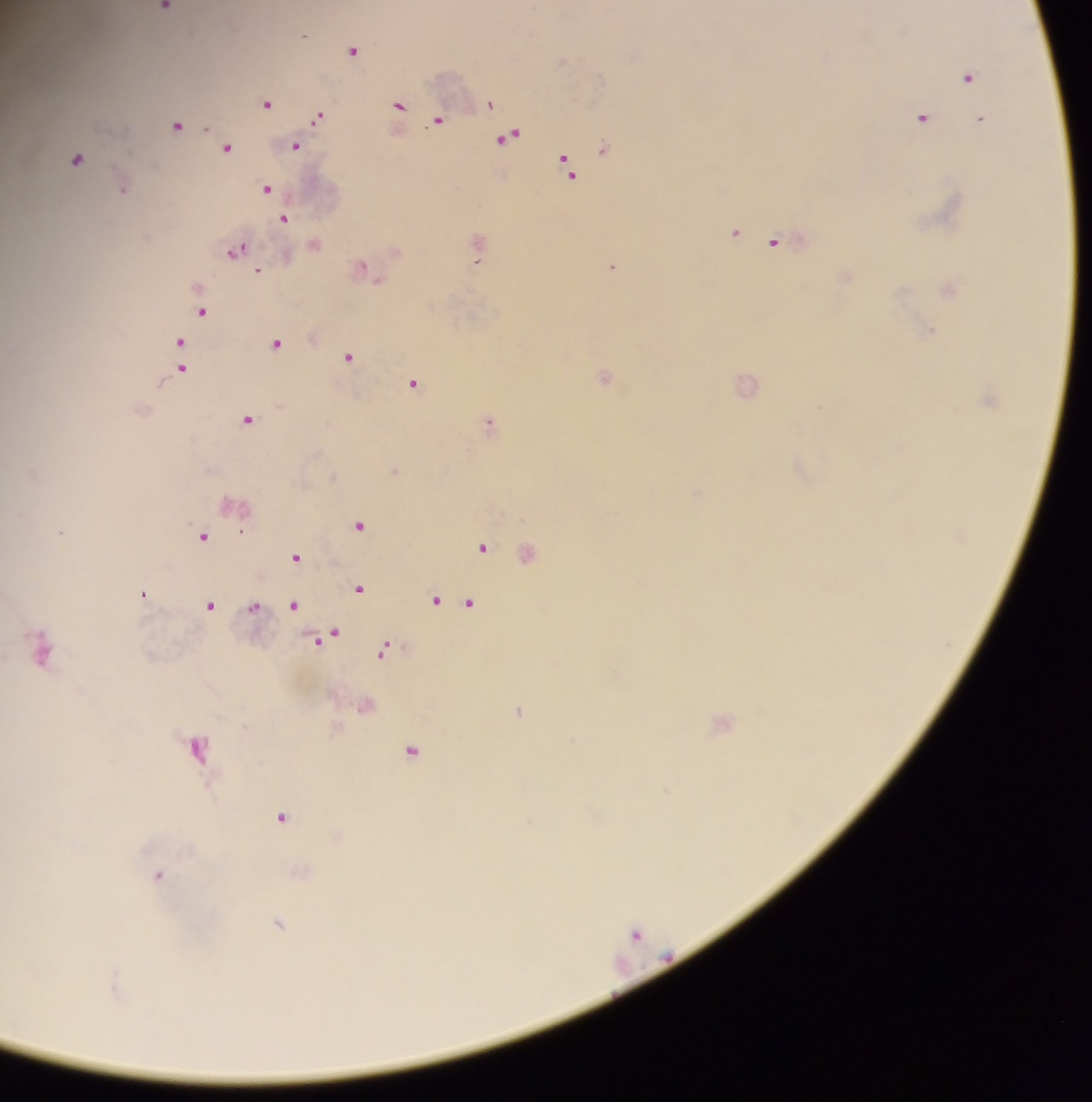
plasmodium_parasite_locations: 'approximate centers as [x, y] in pixels: [165, 8], [305, 36], [353, 51], [968, 77], [267, 104], [491, 104], [400, 105], [319, 116], [922, 118], [981, 119], [439, 120], [177, 125], [508, 137], [295, 147], [604, 147], [227, 148], [77, 160], [568, 165], [267, 189], [123, 190], [285, 219], [736, 232], [775, 242], [237, 250], [477, 263], [613, 266], [364, 268], [259, 272], [203, 312], [277, 343], [178, 344], [181, 357], [349, 357], [181, 369], [605, 377], [414, 383], [747, 384], [248, 419], [490, 423], [360, 526], [241, 531], [61, 532], [204, 536], [483, 548], [296, 557], [359, 589], [143, 594], [437, 600], [471, 602], [294, 605], [210, 606], [254, 607], [329, 637], [41, 650], [383, 650], [519, 711], [725, 723], [197, 748], [411, 751], [281, 817], [158, 876], [279, 925], [636, 934]'
capture: mobile-phone photograph through a microscope
preparation: thick blood film
country: Ghana
field_of_view: single
image_size: 1092×1102 pixels